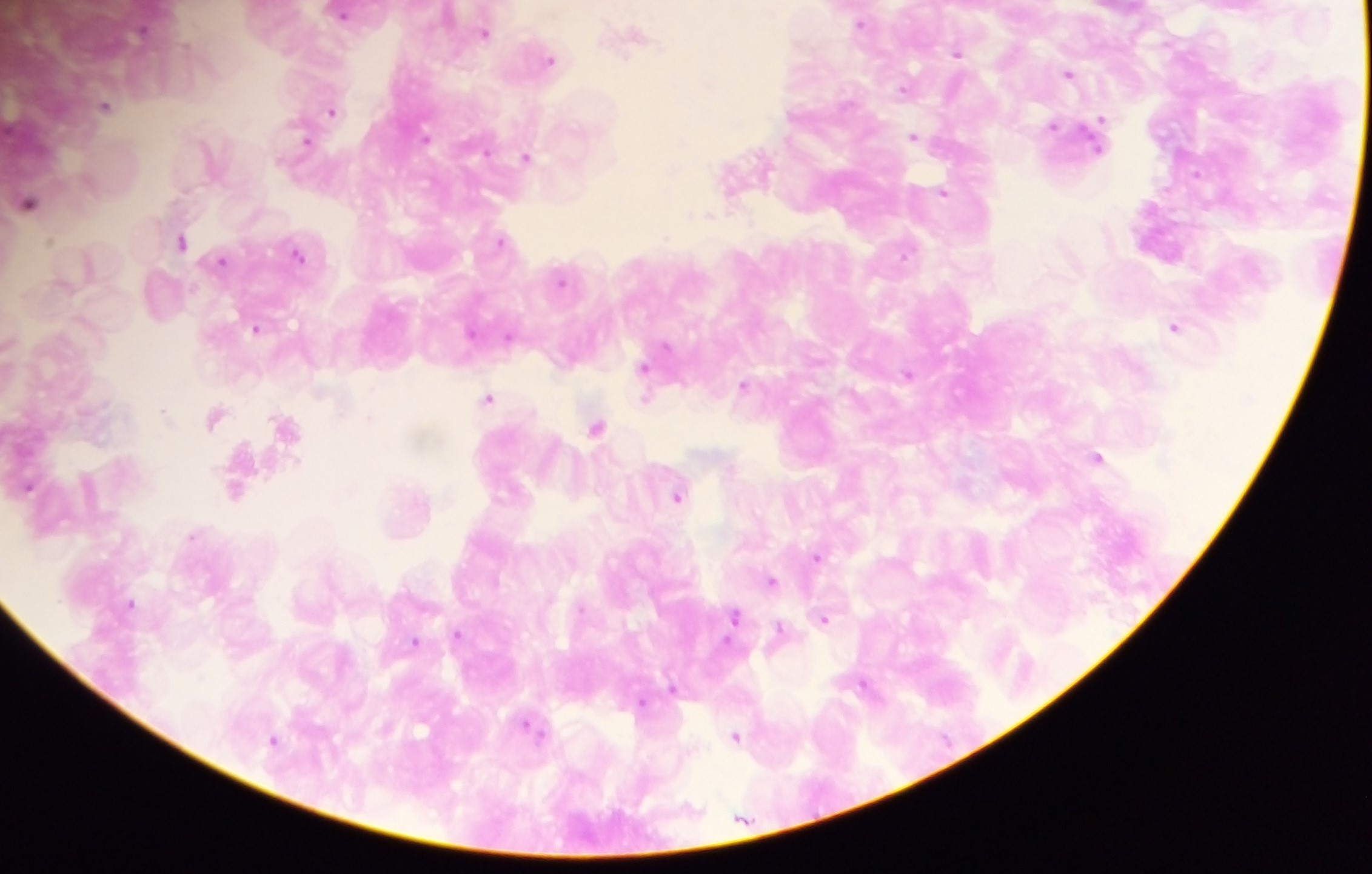
Approximate centers as x y in pixels.
Summary:
  - Plasmodium parasite locations: 343 13; 861 22; 486 32; 631 39; 958 51; 549 58; 1069 73; 904 89; 106 105; 332 110; 1054 127; 915 136; 306 142; 527 157; 764 163; 943 192; 30 202; 665 237; 501 240; 181 241; 296 253; 905 254; 222 260; 562 280; 1175 326; 257 328; 472 332; 509 337; 665 346; 644 368; 909 374; 744 385; 489 399; 646 399; 164 412; 215 417; 285 425; 597 426; 1097 458; 27 487; 236 491; 677 496; 193 535; 817 556; 771 581; 130 603; 734 616; 824 619; 780 629; 458 634; 415 642; 864 685; 672 686; 641 703; 533 731; 736 737; 274 740
  - Image size: 1372×874 pixels
  - Capture: mobile-phone photograph through a microscope
  - Preparation: thick blood smear
  - Field of view: single
  - Country: Ghana